Report the malaria status of this cell.
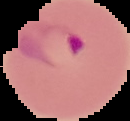

Parasitized.

Summary:
  - Preparation: thin blood smear
  - Image type: segmented cell region with the area outside set to black
  - Image size: 130×121 pixels